Give the preparation type.
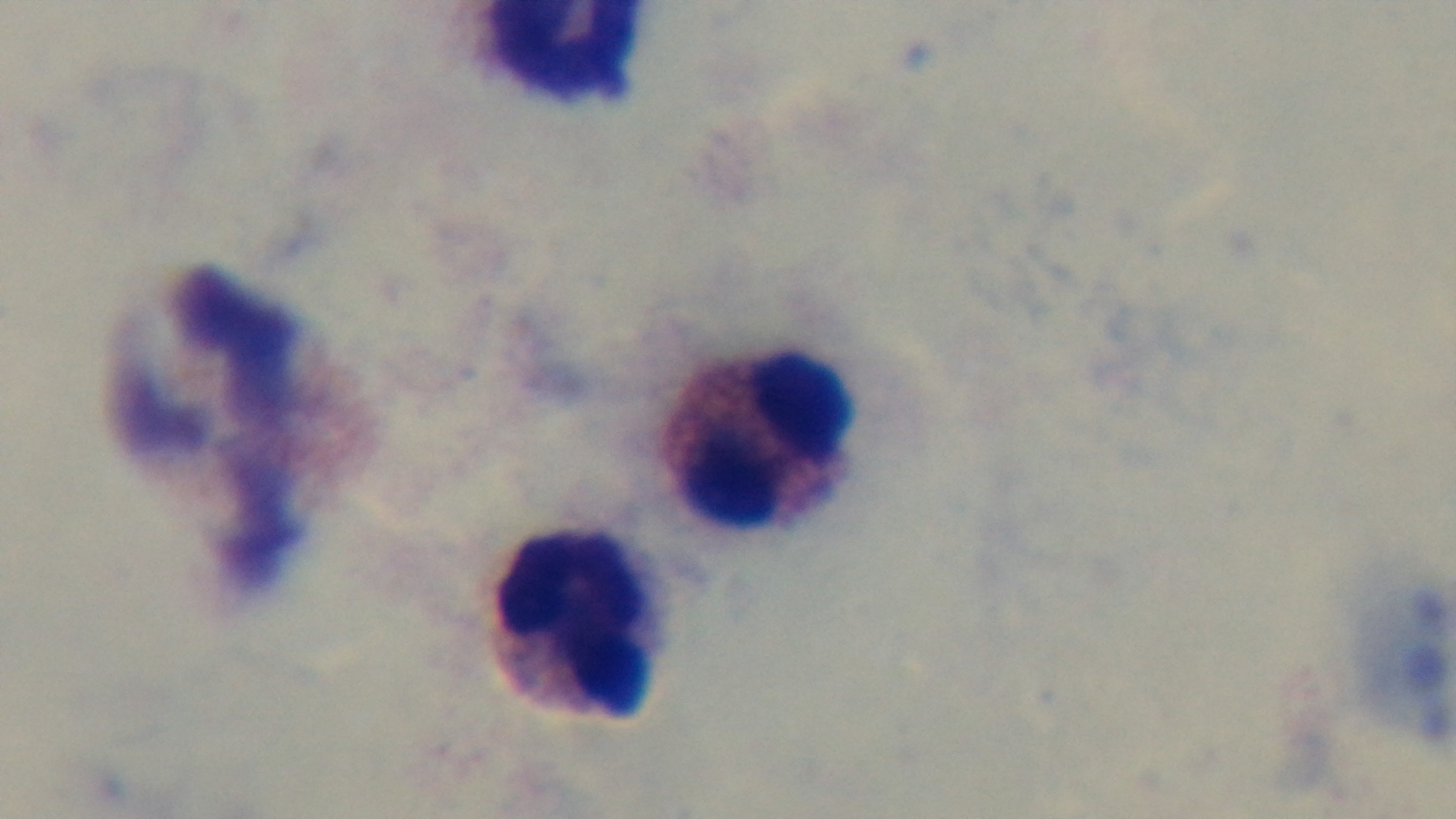
A thick smear.

stain = Giemsa
malaria status = uninfected
field of view = one from the slide
objective = 100x oil immersion
modality = light microscopy
capture = mounted 4K digital camera